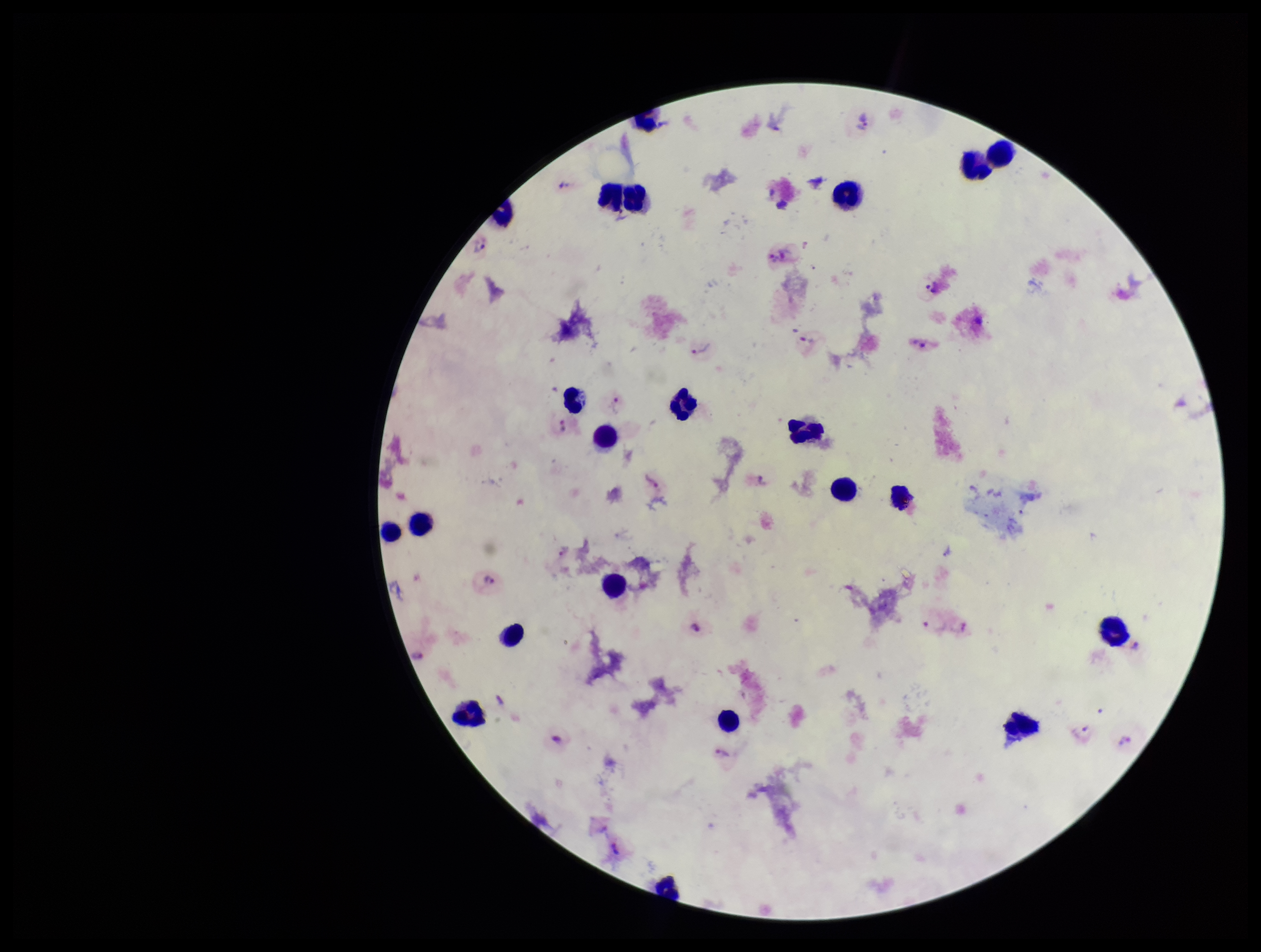
Stained with Giemsa. Patient malaria status: infected. Plasmodium parasites: identified. One field from this slide. Photographed through the microscope eyepiece with a smartphone camera. Leukocyte count: 22. Species reported for this patient: Plasmodium vivax. Parasite count: 10. Image is 1261×952 pixels. Preparation: thick smear.